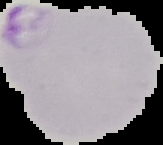 The area outside the segmented cell region is set to black. From a thin blood smear. Image is 163×145 pixels. Malaria status: parasitized.